Give the position of every malaria parasite.
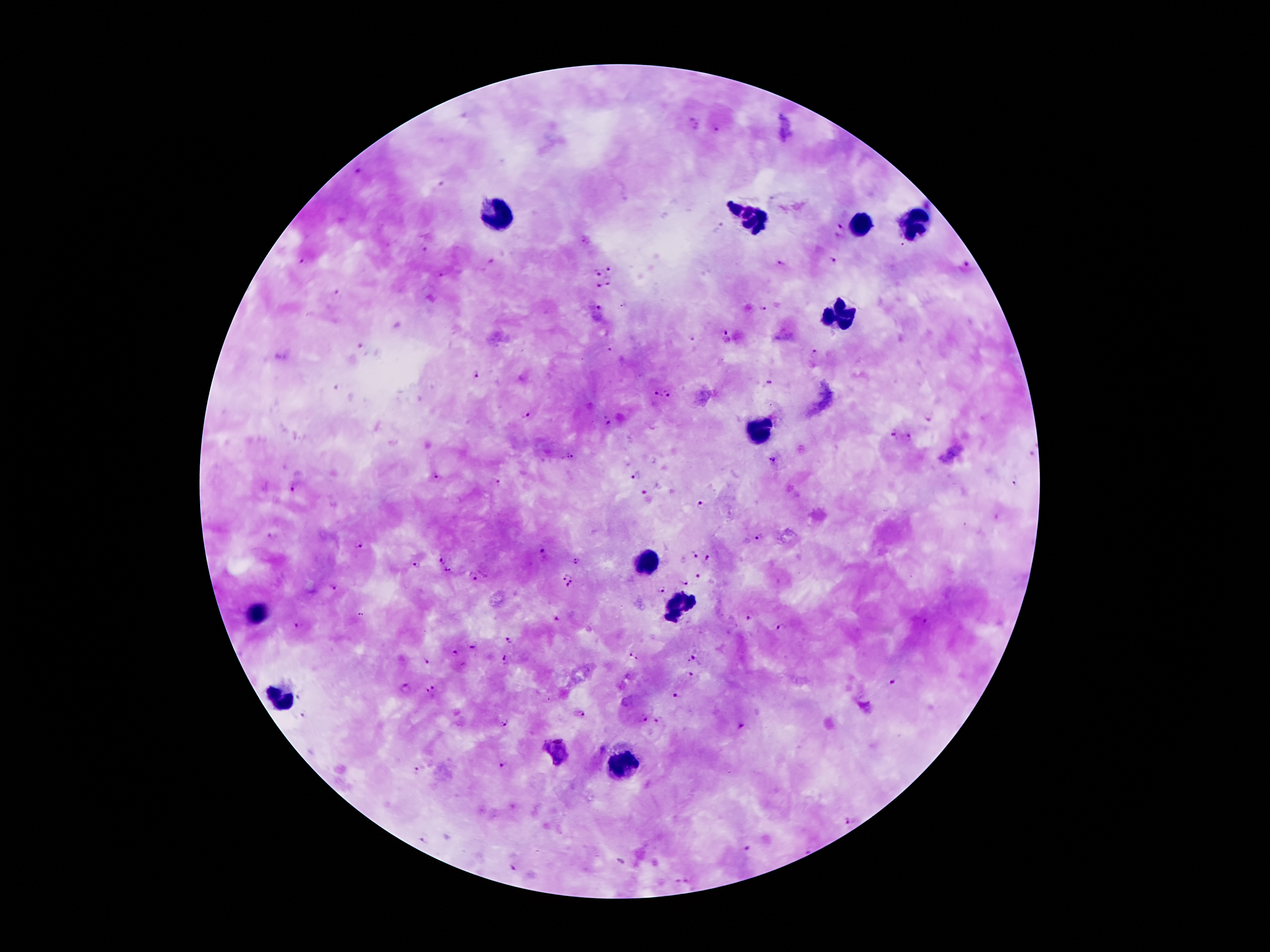

Approximate centers as [x, y] in pixels.
Malaria parasites: [692, 125], [717, 129], [357, 172], [443, 185], [733, 208], [841, 231], [426, 250], [830, 260], [303, 262], [491, 262], [782, 265], [965, 267], [611, 269], [600, 273], [608, 284], [599, 286], [337, 294], [598, 307], [765, 308], [726, 331], [694, 338], [363, 349], [815, 354], [478, 375], [768, 384], [669, 392], [658, 394], [525, 417], [928, 417], [608, 422], [892, 435], [907, 437], [1032, 452], [569, 457], [773, 458], [637, 473], [435, 478], [1013, 479], [501, 483], [294, 488], [643, 491], [702, 504], [271, 537], [760, 538], [357, 547], [542, 555], [696, 558], [445, 560], [709, 560], [577, 563], [417, 565], [448, 570], [699, 574], [472, 577], [568, 580], [683, 585], [332, 587], [661, 591], [749, 616], [295, 626], [783, 628], [512, 636], [471, 644], [454, 653], [635, 656], [693, 658], [507, 661], [426, 662], [688, 676], [893, 681], [406, 689], [431, 691], [301, 693], [679, 694], [580, 714], [302, 716], [642, 719], [500, 720], [658, 722], [743, 728], [553, 749], [501, 765], [418, 771], [850, 821], [426, 839], [748, 848], [512, 868], [683, 882].

Summary:
  - Leukocyte locations: [496, 216], [755, 220], [860, 224], [916, 224], [839, 318], [761, 432], [652, 558], [683, 606], [259, 612], [280, 694], [622, 763]
  - Capture: smartphone through the microscope eyepiece
  - Magnification: 100x
  - Field of view: single
  - Image size: 1270×952 pixels
  - Preparation: thick blood film
  - Stain: Giemsa
  - Patient malaria status: infected with Plasmodium falciparum